State the blood parasite species.
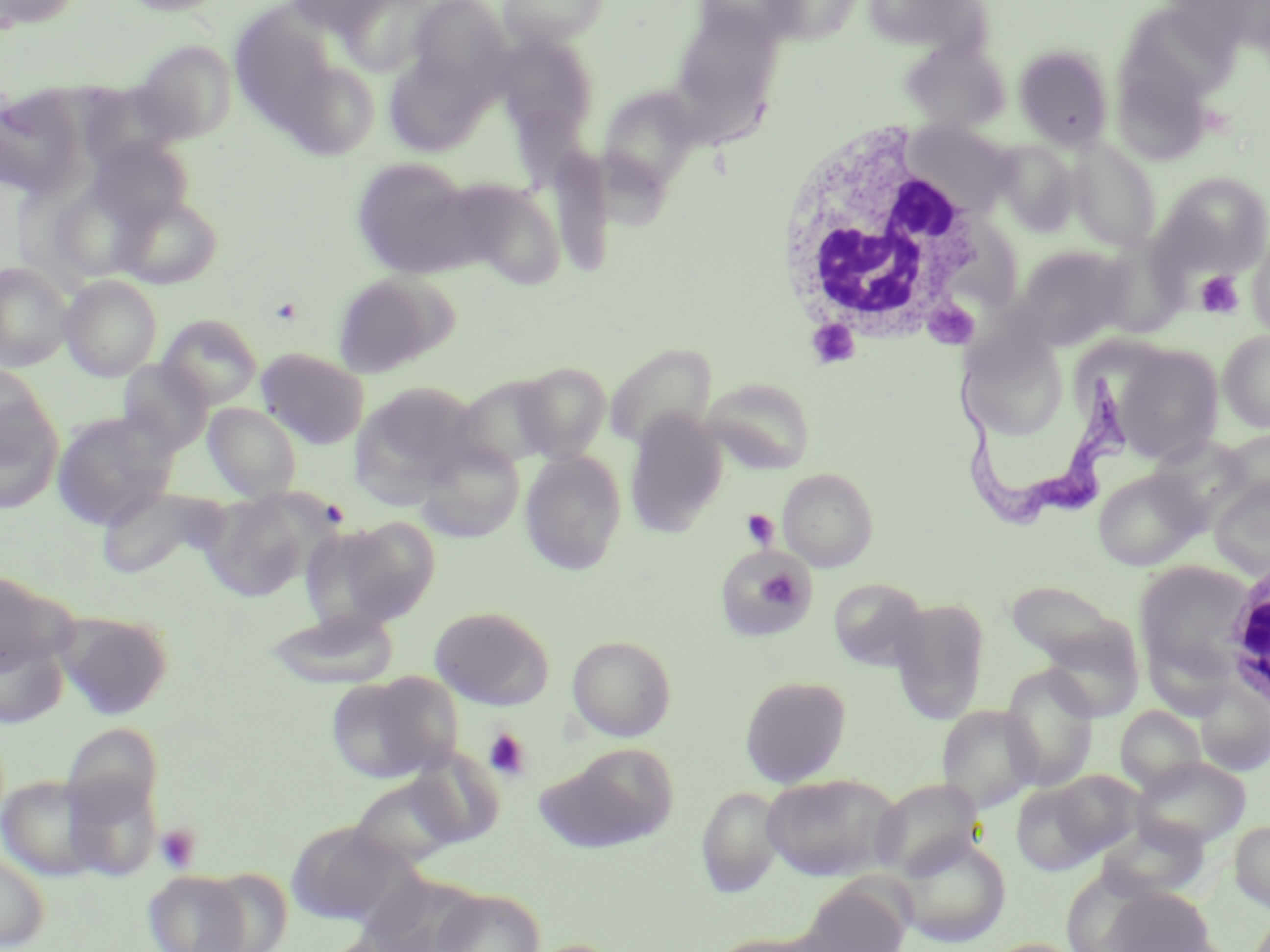

Trypanosoma brucei.

Summary:
  - Coordinate format: approximate bounding boxes as (x1,y1)-(x2,y2) corner pairs in pixels
  - Uninfected red blood cell locations: (0,0)-(83,30), (115,0)-(233,16), (284,0)-(396,36), (337,0)-(441,77), (407,0)-(511,95), (497,0)-(611,46), (692,0)-(809,48), (859,0)-(987,56), (229,6)-(340,127), (1130,6)-(1234,107), (668,7)-(786,137), (496,33)-(598,142), (133,40)-(239,144), (900,40)-(1010,132), (1014,44)-(1114,151), (383,51)-(492,156), (1114,51)-(1214,163), (279,58)-(381,159), (597,85)-(705,192), (1,87)-(88,199), (903,120)-(1019,218), (86,136)-(195,230), (1068,138)-(1162,252), (993,140)-(1080,235), (350,157)-(484,280), (1157,172)-(1270,276), (449,179)-(567,289), (117,192)-(223,289), (47,196)-(154,281), (1248,230)-(1270,341), (1105,242)-(1186,338), (1010,246)-(1130,351), (0,261)-(73,373), (331,272)-(449,378), (60,274)-(162,381), (158,314)-(262,408), (958,327)-(1070,444), (1218,330)-(1270,433), (1113,342)-(1224,463), (604,343)-(716,452), (256,348)-(370,449), (117,359)-(213,454), (515,362)-(611,463), (0,363)-(55,466), (453,375)-(562,471), (701,378)-(817,473), (355,382)-(475,498), (0,399)-(64,514), (202,403)-(303,501), (624,410)-(727,537), (51,411)-(179,530), (1217,428)-(1270,513), (416,438)-(526,542), (520,451)-(626,575), (778,467)-(878,571), (1092,468)-(1203,571), (1209,475)-(1270,578), (95,485)-(231,579), (197,489)-(326,602), (339,516)-(441,624), (298,523)-(411,633), (716,545)-(814,640), (1134,560)-(1255,684), (0,569)-(73,677), (829,578)-(929,671), (1005,578)-(1142,693), (888,597)-(990,723), (430,605)-(554,709), (55,609)-(175,719), (264,609)-(400,688), (0,634)-(69,729), (567,635)-(677,742), (1000,665)-(1099,792), (326,672)-(460,784), (740,675)-(851,788), (1196,683)-(1270,776), (937,705)-(1041,813), (1115,706)-(1206,793), (61,722)-(163,821), (544,744)-(680,851), (405,749)-(506,850), (1133,756)-(1251,849), (1050,769)-(1145,856), (62,770)-(163,883), (761,772)-(904,881), (0,774)-(106,882), (348,775)-(468,869), (871,778)-(985,881), (1011,782)-(1105,876), (696,785)-(785,898), (1097,818)-(1208,902), (285,820)-(411,925), (1230,820)-(1270,912), (894,835)-(1012,947), (0,851)-(51,951), (198,866)-(294,952), (143,870)-(252,952), (798,881)-(911,952), (1100,885)-(1215,951), (433,888)-(546,952), (705,931)-(833,952), (519,938)-(629,952), (983,938)-(1084,952)
  - Platelet locations: (1195,270)-(1244,319), (741,509)-(780,550), (759,568)-(800,608), (483,728)-(532,781), (154,824)-(201,874)
  - Trypanosoma brucei locations: (953,362)-(1131,530)
  - White blood cell locations: (774,121)-(996,348), (1220,559)-(1270,717)
  - Modality: light microscopy
  - Preparation: thin blood smear
  - Stain: May-Grünwald-Giemsa
  - Magnification: 1000x
  - Field of view: one of a larger specimen
  - Image size: 1270×952 pixels